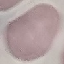
{
  "malaria_status": "uninfected",
  "preparation": "thin blood film",
  "capture": "smartphone through the microscope eyepiece",
  "stain": "Giemsa",
  "image_type": "cell patch, automatically extracted from a larger field of view and resized to 64 × 64 pixels"
}